Classify this cell by malaria status.
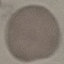
Uninfected.

capture = smartphone through the microscope eyepiece
stain = Giemsa
image type = cell patch, automatically extracted from a larger field of view and resized to 64 × 64 pixels
preparation = thin blood film